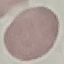

{
  "malaria_status": "uninfected",
  "stain": "Giemsa",
  "preparation": "thin smear",
  "image_type": "automatically extracted cell patch, resized to 64 × 64 pixels",
  "capture": "smartphone camera at the microscope eyepiece"
}